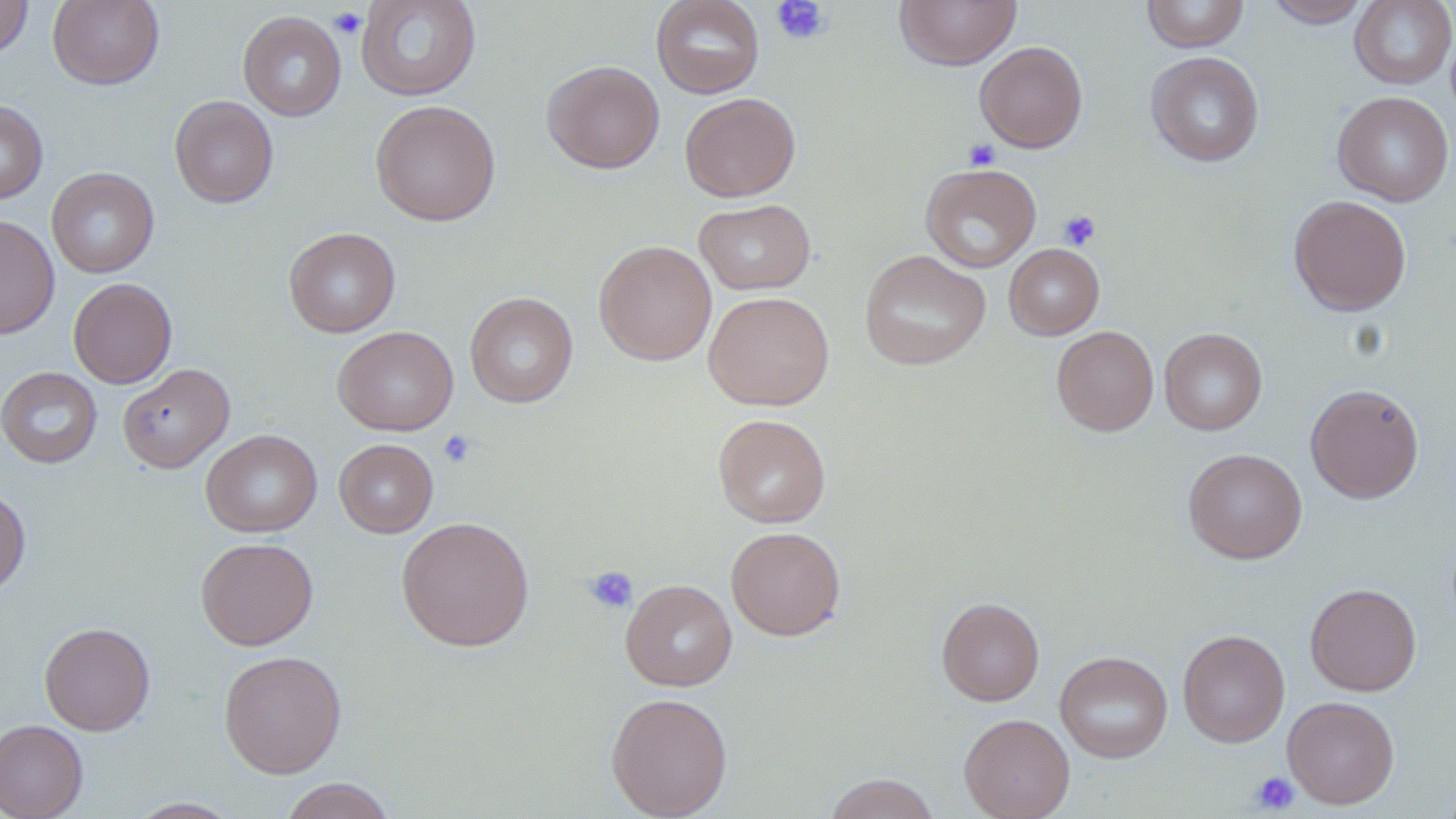
Approximate bounding boxes as named x1/y1/x2/y2 corners in pixels. Platelet locations: (x1=771, y1=0, x2=830, y2=45), (x1=328, y1=7, x2=366, y2=39), (x1=963, y1=139, x2=1001, y2=172), (x1=1058, y1=209, x2=1101, y2=250), (x1=438, y1=430, x2=477, y2=467), (x1=584, y1=566, x2=638, y2=614), (x1=1249, y1=771, x2=1300, y2=814). Uninfected red blood cell locations: (x1=47, y1=0, x2=164, y2=90), (x1=356, y1=0, x2=482, y2=101), (x1=650, y1=0, x2=765, y2=99), (x1=894, y1=0, x2=1022, y2=71), (x1=1141, y1=0, x2=1250, y2=52), (x1=1263, y1=0, x2=1372, y2=28), (x1=1349, y1=0, x2=1456, y2=89), (x1=0, y1=1, x2=33, y2=58), (x1=238, y1=10, x2=347, y2=121), (x1=975, y1=41, x2=1088, y2=152), (x1=1146, y1=51, x2=1265, y2=167), (x1=542, y1=60, x2=664, y2=173), (x1=1332, y1=91, x2=1454, y2=207), (x1=680, y1=93, x2=801, y2=202), (x1=169, y1=95, x2=279, y2=208), (x1=0, y1=99, x2=48, y2=205), (x1=370, y1=99, x2=501, y2=226), (x1=920, y1=163, x2=1041, y2=273), (x1=47, y1=167, x2=159, y2=278), (x1=1288, y1=195, x2=1412, y2=316), (x1=694, y1=199, x2=816, y2=295), (x1=0, y1=215, x2=60, y2=339), (x1=284, y1=227, x2=401, y2=338), (x1=594, y1=240, x2=717, y2=365), (x1=1004, y1=244, x2=1104, y2=339), (x1=859, y1=250, x2=991, y2=370), (x1=68, y1=278, x2=177, y2=388), (x1=704, y1=290, x2=834, y2=411), (x1=465, y1=291, x2=578, y2=408), (x1=332, y1=326, x2=459, y2=436), (x1=1051, y1=326, x2=1159, y2=436), (x1=1159, y1=328, x2=1267, y2=435), (x1=117, y1=363, x2=234, y2=474), (x1=0, y1=366, x2=102, y2=468), (x1=1305, y1=383, x2=1425, y2=504), (x1=713, y1=413, x2=830, y2=528), (x1=200, y1=429, x2=322, y2=537), (x1=334, y1=438, x2=438, y2=538), (x1=1183, y1=448, x2=1307, y2=564), (x1=0, y1=488, x2=31, y2=597), (x1=396, y1=516, x2=534, y2=651), (x1=726, y1=525, x2=846, y2=640), (x1=196, y1=537, x2=318, y2=650), (x1=620, y1=579, x2=736, y2=692), (x1=1305, y1=582, x2=1421, y2=696), (x1=936, y1=596, x2=1044, y2=706), (x1=40, y1=622, x2=155, y2=736), (x1=1178, y1=629, x2=1289, y2=747), (x1=218, y1=649, x2=347, y2=778), (x1=1054, y1=651, x2=1173, y2=763), (x1=605, y1=692, x2=733, y2=819), (x1=1283, y1=695, x2=1400, y2=808), (x1=959, y1=713, x2=1075, y2=819), (x1=0, y1=719, x2=88, y2=819), (x1=823, y1=773, x2=942, y2=819), (x1=277, y1=777, x2=399, y2=819), (x1=127, y1=798, x2=242, y2=818). Slide-level diagnosis: no evidence of blood parasites. Image is 1456×819 pixels. Optical microscopy. Thin blood smear. One field of a larger specimen. 1000x magnification. May-Grünwald-Giemsa stain.